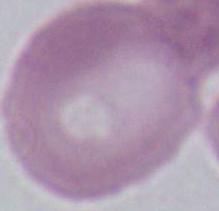

modality = micrograph
magnification = 1000x
identification = erythrocyte